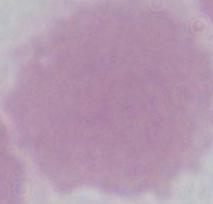
modality = photomicrograph
magnification = 1000x
identification = red blood cell